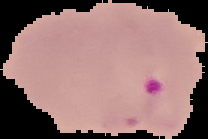 Result: malaria parasites detected. Segmented cell region on a black background. From a thin blood smear. Image is 208×139 pixels.